Assess this cell for malaria.
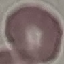

It is uninfected.

Summary:
  - Image type: cell patch, automatically extracted from a larger field of view and resized to 64 × 64 pixels
  - Stain: Giemsa
  - Capture: smartphone through the microscope eyepiece
  - Preparation: thin smear